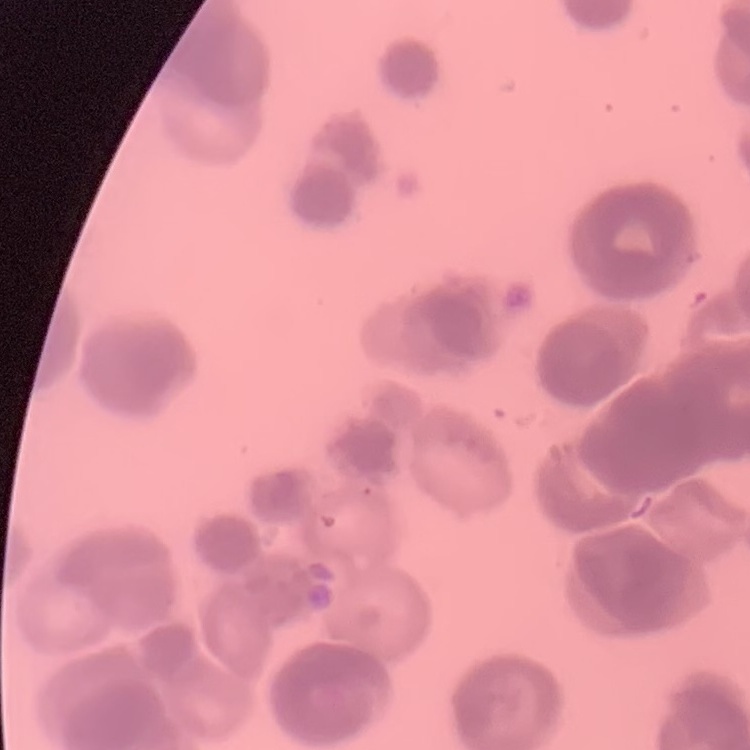

The erythrocytes exhibit rouleaux formation. Stained with either Field's or Giemsa. Thin blood film. One tile cut from a larger photomicrograph.